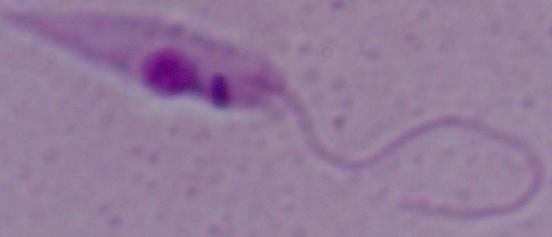

Summary:
  - Identification: Leishmania
  - Modality: micrograph
  - Magnification: 1000x